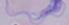

Photomicrograph. 1000x magnification. A trypanosome is shown.